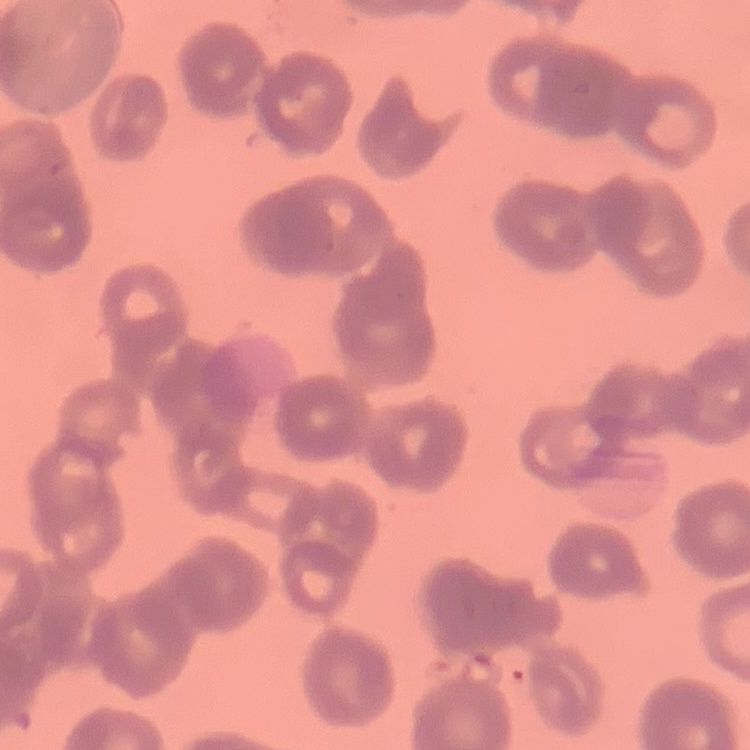

The red blood cells exhibit rouleaux formation. Thin peripheral smear. Field's or Giemsa stain. One tile cut from a larger photomicrograph.